State the preparation type.
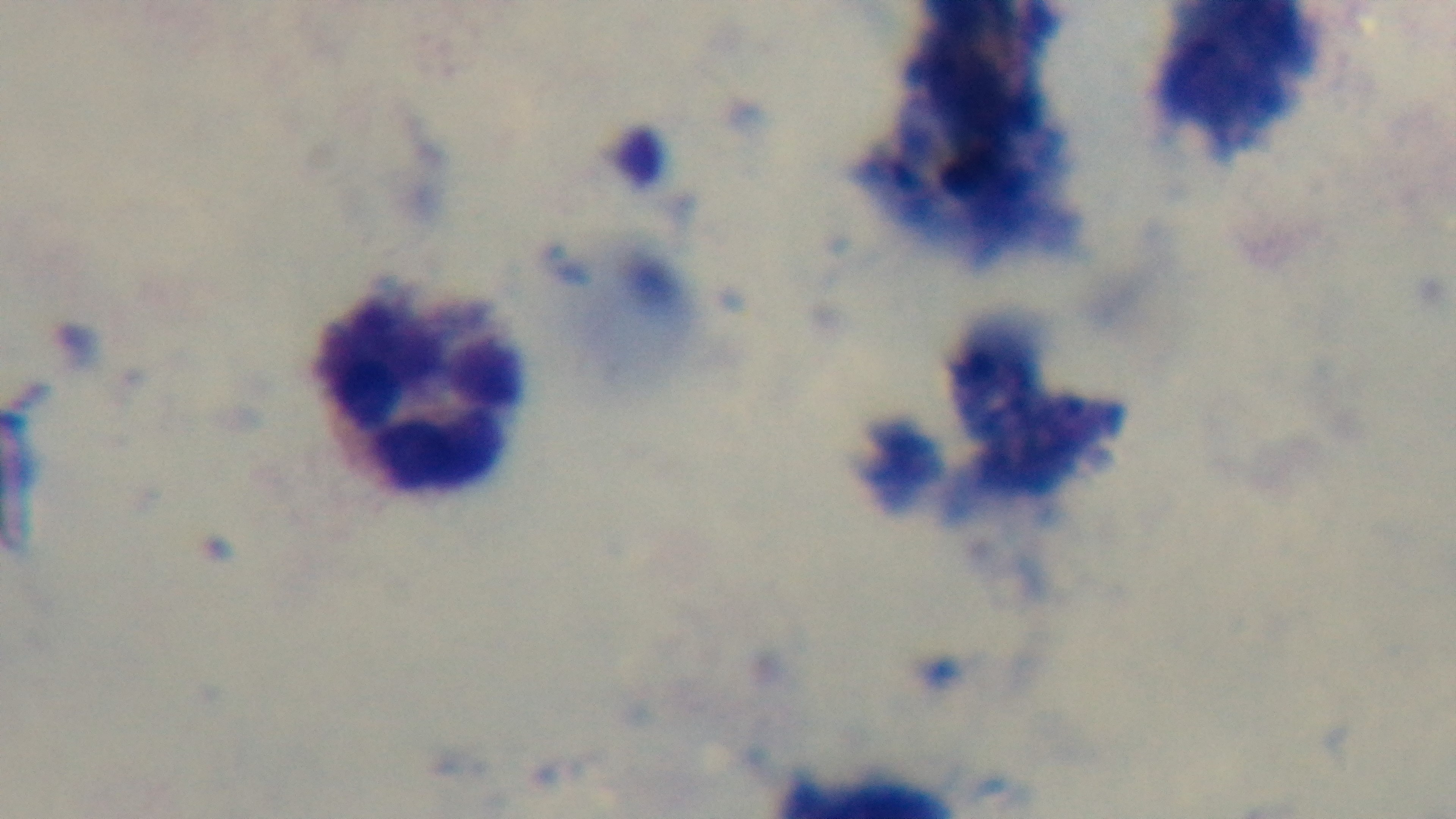
A thick smear.

Summary:
  - Capture: mounted 4K digital camera
  - Malaria status: uninfected
  - Field of view: one from the slide
  - Stain: Giemsa
  - Modality: light microscopy
  - Objective: 100x oil immersion